Name the blood parasite species.
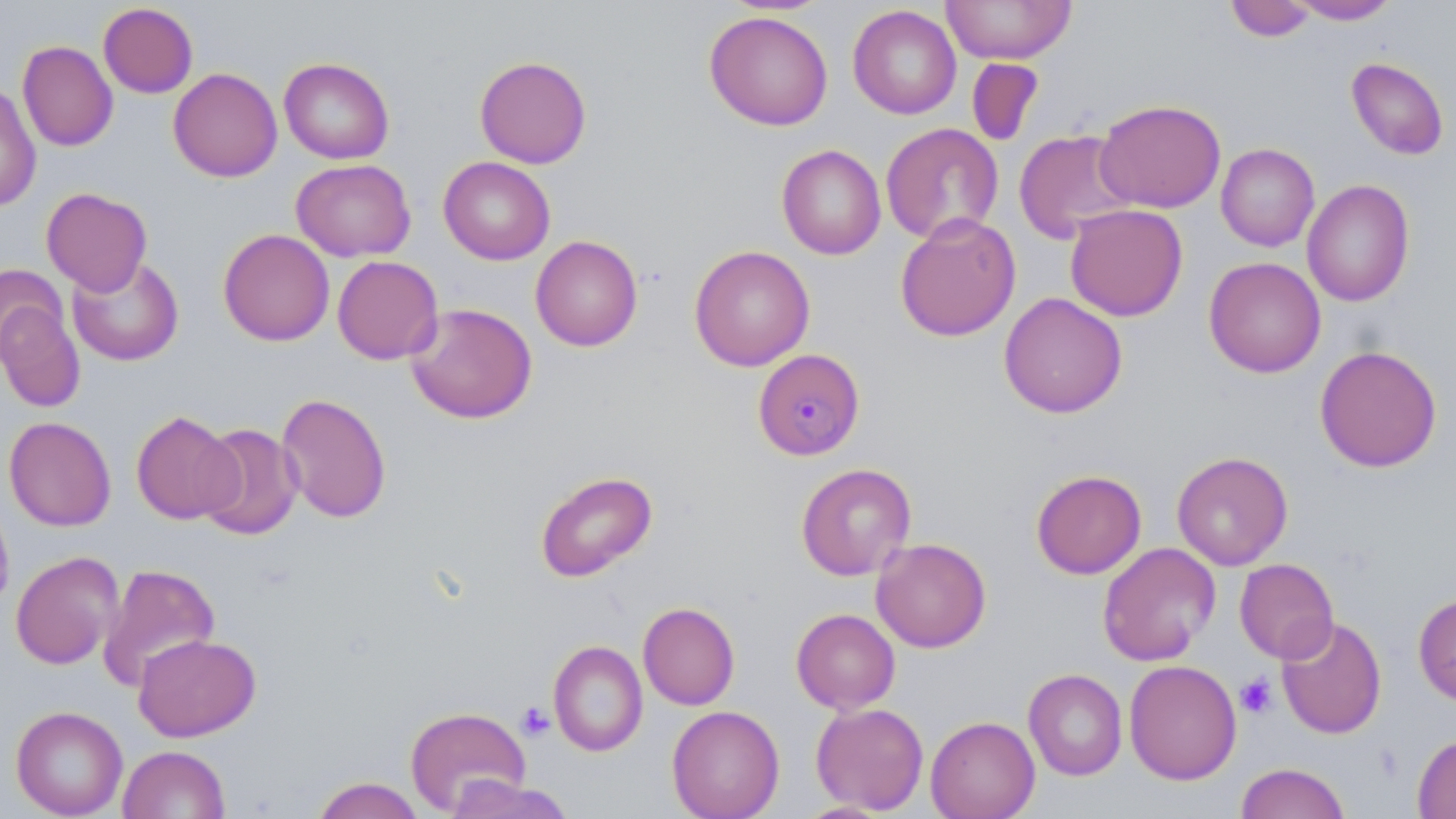
Plasmodium malariae.

stain = May-Grünwald-Giemsa
image size = 1456×819 pixels
uninfected red blood cell locations = approximate bounding boxes as (x1, y1, x2, y2) in pixels: (941, 0, 1077, 65), (1224, 0, 1318, 42), (1287, 0, 1401, 24), (98, 3, 198, 98), (847, 5, 962, 120), (704, 10, 834, 131), (17, 41, 118, 152), (474, 56, 592, 168), (278, 57, 395, 164), (966, 57, 1044, 147), (1345, 57, 1449, 161), (168, 67, 282, 182), (0, 84, 41, 211), (1094, 98, 1227, 213), (880, 123, 1004, 244), (1013, 129, 1138, 244), (1215, 143, 1320, 252), (776, 144, 886, 260), (438, 157, 555, 265), (291, 158, 416, 262), (1302, 179, 1415, 307), (41, 187, 152, 295), (1065, 204, 1188, 321), (895, 213, 1021, 342), (218, 229, 335, 346), (530, 235, 643, 351), (689, 245, 815, 371), (67, 256, 184, 366), (332, 256, 444, 364), (1203, 256, 1326, 378), (0, 264, 67, 363), (999, 292, 1127, 418), (0, 299, 86, 413), (405, 302, 538, 424), (1314, 344, 1443, 473), (276, 392, 392, 524), (131, 410, 241, 524), (3, 416, 117, 532), (196, 423, 303, 541), (1171, 451, 1293, 570), (796, 462, 916, 581), (1031, 469, 1147, 579), (535, 470, 657, 582), (0, 497, 14, 614), (870, 537, 991, 653), (1097, 542, 1221, 666), (10, 550, 123, 669), (1234, 558, 1339, 663), (97, 563, 220, 692), (1412, 592, 1456, 706), (638, 602, 740, 710), (790, 608, 900, 713), (1276, 616, 1387, 739), (133, 633, 261, 741), (548, 640, 648, 756), (1123, 659, 1242, 785), (1023, 668, 1127, 780), (811, 702, 929, 814), (10, 705, 128, 818), (666, 705, 784, 818), (405, 706, 531, 816), (925, 715, 1040, 819), (1412, 733, 1456, 819), (118, 744, 230, 819), (1235, 762, 1351, 819), (444, 775, 575, 819), (311, 776, 425, 819)
platelet locations = approximate bounding boxes as (x1, y1, x2, y2) in pixels: (1235, 672, 1277, 718), (517, 701, 555, 740)
field of view = one of a larger specimen
modality = optical microscopy
Plasmodium malariae-infected red blood cell locations = approximate bounding boxes as (x1, y1, x2, y2) in pixels: (757, 349, 862, 462)
preparation = thin blood smear
magnification = 1000x